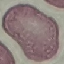
Malaria status: uninfected. Photographed with a smartphone camera at the microscope eyepiece. Giemsa-stained preparation. Cell patch, automatically extracted from a larger field of view and resized to 64 × 64 pixels. Thin blood film.